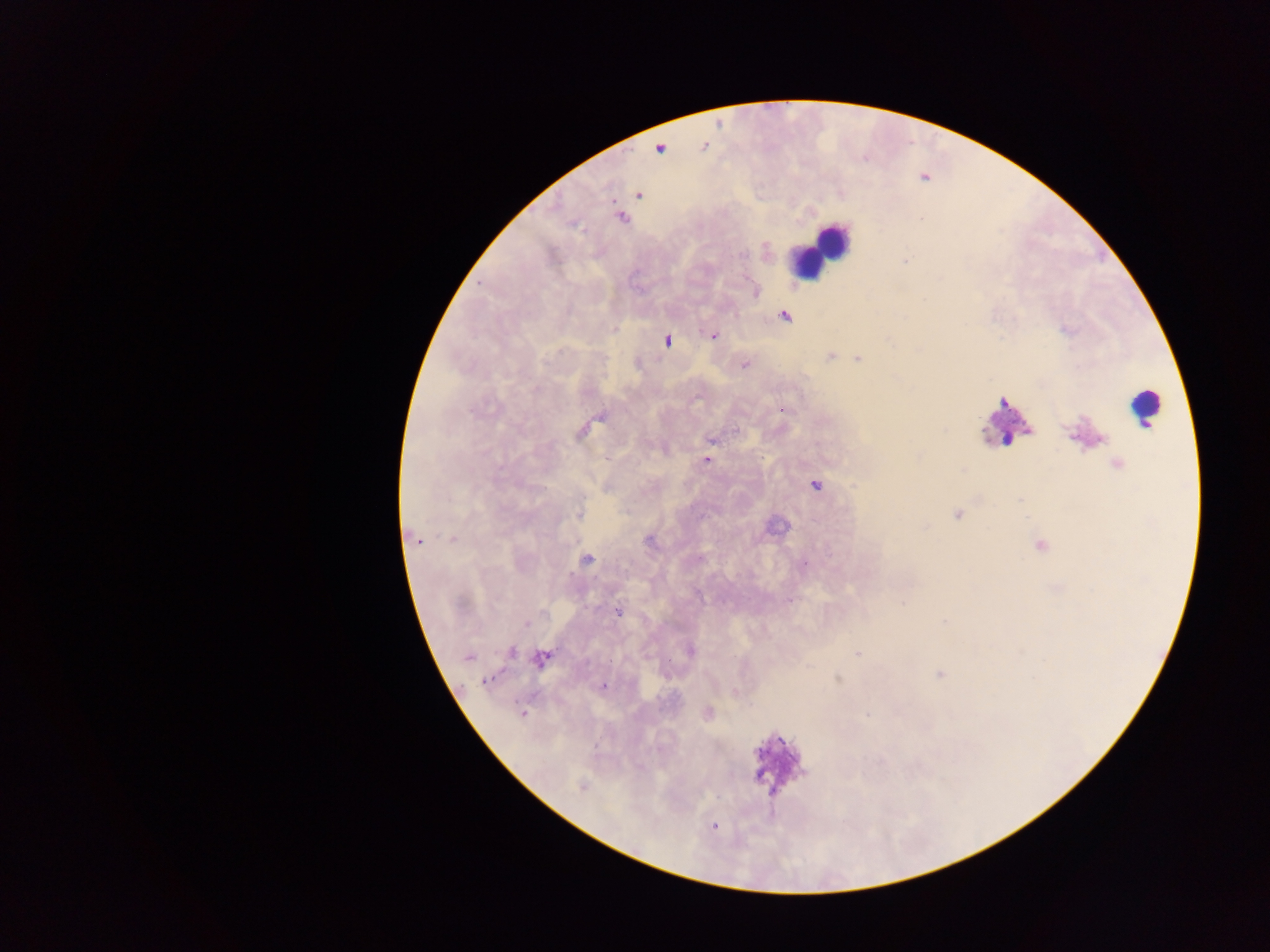

{
  "preparation": "thick blood smear",
  "malaria_parasite_locations": "approximate centers as [x, y] in pixels: [638, 194], [622, 218], [785, 316], [713, 335], [666, 341], [830, 357], [857, 358], [744, 365], [782, 409], [601, 416], [711, 441], [606, 459], [707, 460], [815, 485], [957, 514], [579, 515], [452, 539], [418, 541], [587, 559], [805, 564], [790, 601], [903, 603], [617, 611], [526, 624], [691, 651], [511, 652], [858, 654], [468, 657], [541, 658], [940, 674], [486, 681], [604, 686], [734, 691], [522, 713], [708, 713], [867, 715], [582, 785], [715, 826]",
  "leukocyte_locations": "approximate centers as [x, y] in pixels: [831, 240], [807, 260], [1141, 406], [1001, 425]",
  "country": "Ghana",
  "field_of_view": "single",
  "capture": "mobile-phone photograph through a microscope",
  "image_size": "1270×952 pixels"
}